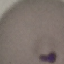
Summary:
  - Malaria status: parasitized
  - Stain: Giemsa
  - Capture: smartphone camera at the microscope eyepiece
  - Preparation: thin smear
  - Image type: cell patch, automatically extracted from a larger field of view and resized to 64 × 64 pixels